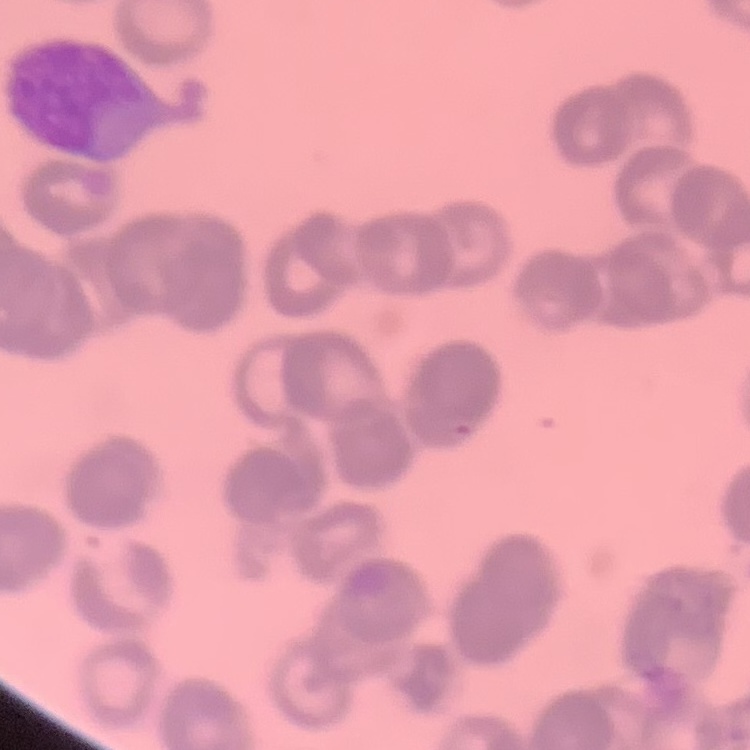

{
  "erythrocyte_morphology": "rouleaux formation",
  "preparation": "thin blood smear",
  "image_type": "one tile cut from a larger photomicrograph",
  "stain": "Field's or Giemsa"
}